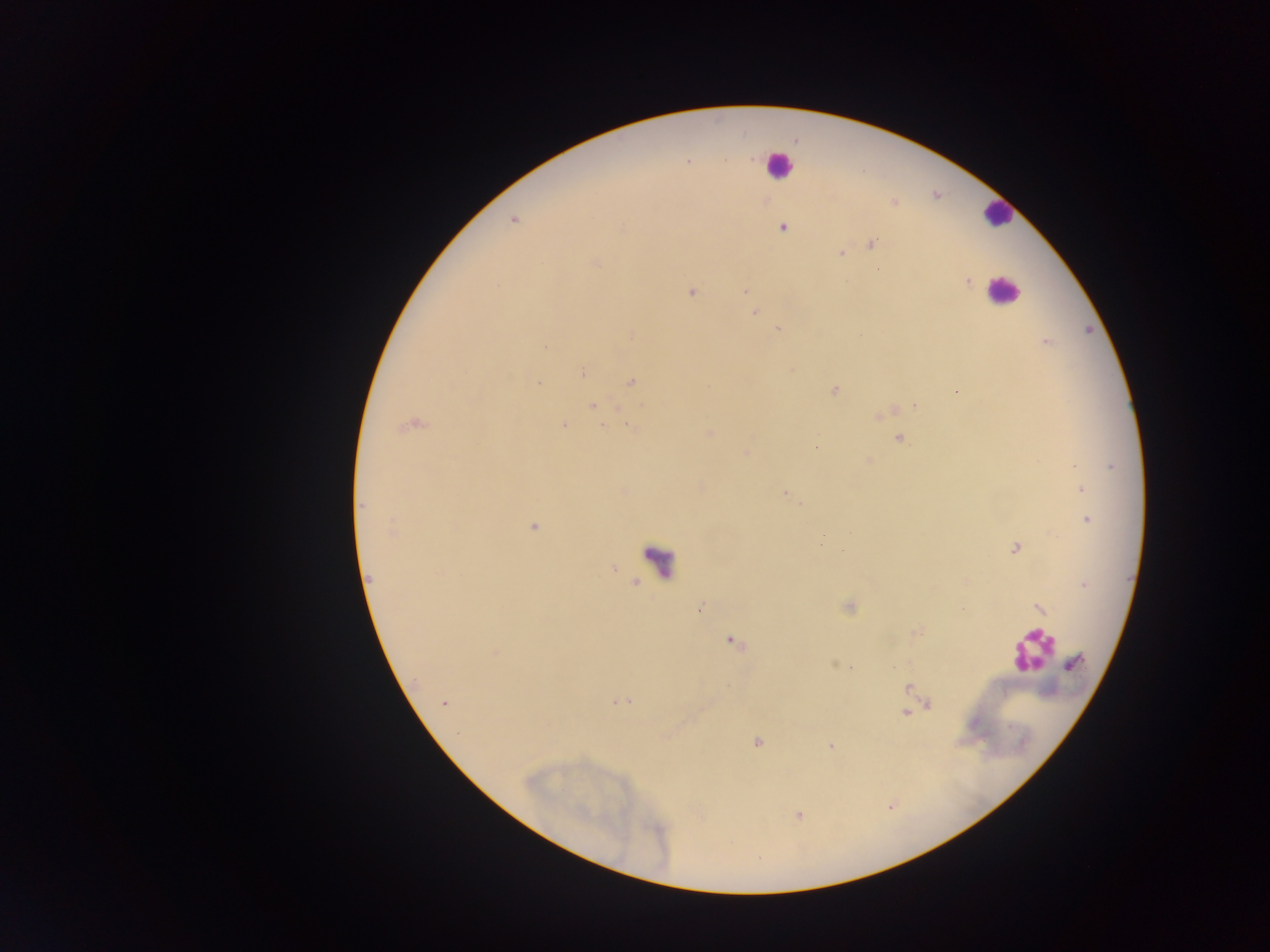

Approximate centers as [x, y] in pixels.
Summary:
  - Leukocyte locations: [777, 165], [997, 214], [1003, 292], [659, 560], [1032, 650]
  - Malaria parasite locations: [687, 162], [513, 220], [782, 227], [870, 243], [841, 252], [595, 262], [966, 280], [692, 291], [745, 291], [754, 311], [778, 328], [631, 335], [1046, 342], [544, 346], [582, 372], [631, 382], [537, 384], [835, 390], [957, 391], [593, 406], [915, 406], [879, 415], [412, 423], [563, 424], [631, 426], [709, 433], [899, 439], [815, 447], [746, 452], [868, 460], [1082, 489], [624, 491], [785, 493], [1086, 519], [533, 526], [391, 531], [1015, 548], [843, 551], [612, 567], [369, 579], [637, 583], [1084, 583], [849, 606], [1039, 607], [700, 608], [916, 631], [731, 640], [495, 653], [834, 662], [1075, 662], [852, 668], [909, 689], [620, 702], [444, 703], [927, 703], [910, 710], [906, 712], [756, 741], [830, 746], [797, 814]
  - Country: Ghana
  - Preparation: thick blood film
  - Image size: 1270×952 pixels
  - Field of view: single
  - Capture: mobile-phone photograph through a microscope